Classify this cell by malaria status.
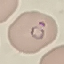

It is parasitized.

Photographed with a smartphone camera at the microscope eyepiece. Cell patch, automatically extracted from a larger field of view and resized to 64 × 64 pixels. Giemsa-stained preparation. Thin smear of blood.